Locate every malaria parasite.
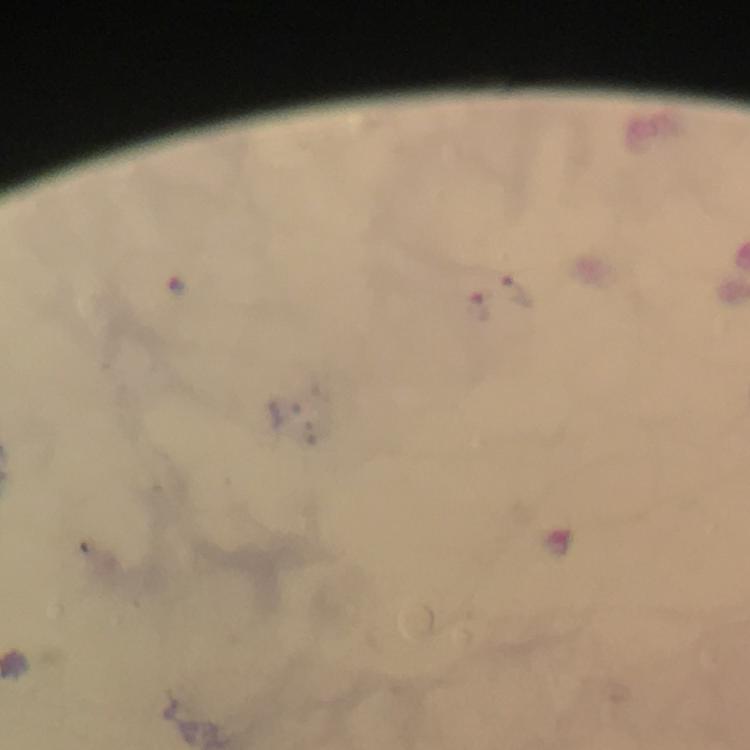
Approximate centers as [x, y] in pixels.
Malaria parasites: [515, 291], [475, 305].

Summary:
  - Context: from a malaria diagnostic workup
  - Image size: 750×750 pixels
  - Capture: smartphone camera through the microscope
  - Stain: Giemsa
  - Magnification: 100x
  - Immersion oil: used
  - Cropped from: one field of view
  - Preparation: thick smear